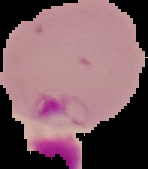

Summary:
  - Image type: segmented cell region on a black background
  - Image size: 148×169 pixels
  - Preparation: thin blood smear
  - Result: Plasmodium parasites detected